Name the parasite shown.
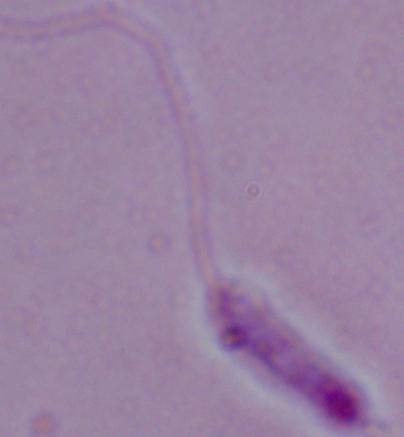

Leishmania.

magnification = 1000x
modality = photomicrograph